Name the parasite shown.
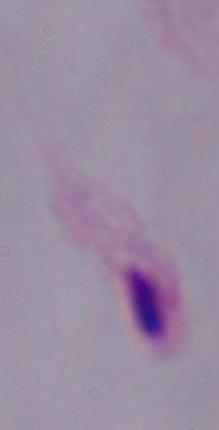
This is a trichomonad.

magnification = 1000x
modality = photomicrograph